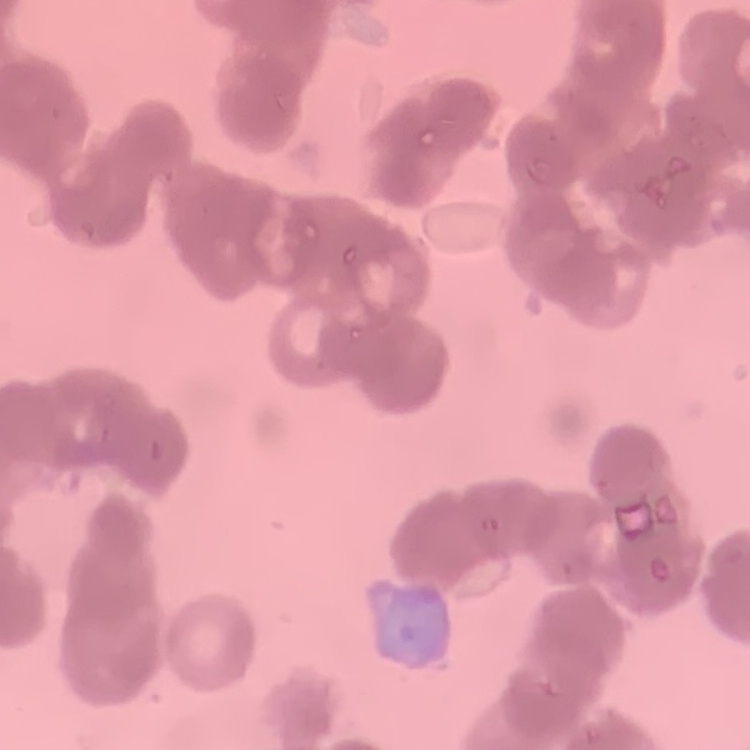
Summary:
  - Erythrocyte morphology: rouleaux formation
  - Preparation: thin blood film
  - Image type: square crop of a larger photomicrograph
  - Stain: Field's or Giemsa